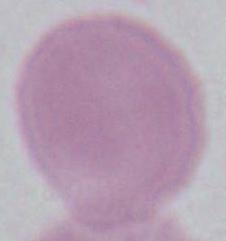 Micrograph. An erythrocyte is shown. 1000x magnification.